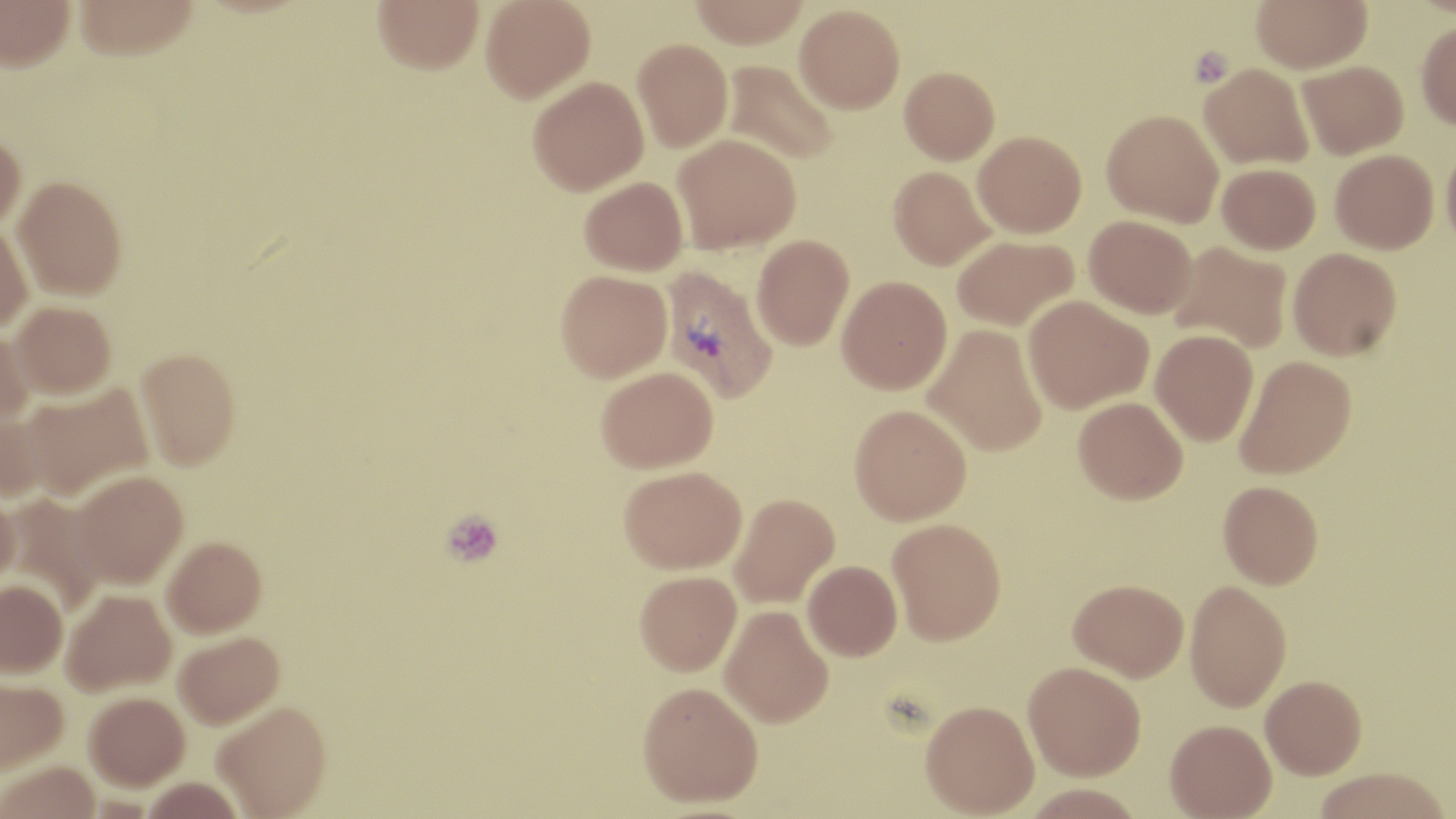
Approximate bounding boxes as (x1,y1)-(x2,y2) corner pairs in pixels. Uninfected red blood cell locations: (1,0)-(75,71), (72,0)-(199,61), (373,0)-(484,73), (481,0)-(595,102), (689,0)-(809,48), (1251,0)-(1372,73), (794,4)-(905,113), (1416,21)-(1456,130), (633,38)-(733,151), (722,60)-(839,165), (1298,60)-(1408,159), (1199,62)-(1314,169), (899,66)-(999,164), (527,75)-(648,195), (1102,108)-(1224,227), (973,130)-(1086,237), (0,131)-(26,234), (672,133)-(801,252), (1440,138)-(1456,254), (1330,149)-(1438,253), (1217,163)-(1321,254), (888,166)-(994,270), (13,175)-(127,298), (580,176)-(688,275), (1085,214)-(1197,318), (0,222)-(33,333), (752,234)-(854,350), (952,234)-(1078,331), (1169,241)-(1293,353), (1287,247)-(1402,360), (555,269)-(672,382), (837,275)-(952,394), (1023,295)-(1152,413), (11,301)-(116,399), (923,324)-(1047,455), (0,328)-(33,432), (1151,329)-(1259,446), (135,347)-(241,469), (1235,355)-(1356,479), (597,366)-(718,472), (23,384)-(153,502), (1074,397)-(1188,504), (849,404)-(972,525), (0,411)-(49,504), (619,465)-(747,574), (71,471)-(188,589), (1218,480)-(1323,589), (0,491)-(19,595), (729,492)-(840,608), (3,495)-(107,616), (887,518)-(1006,645), (162,537)-(267,638), (803,560)-(902,660), (635,570)-(742,675), (0,579)-(67,678), (1069,579)-(1188,681), (1185,580)-(1291,711), (61,589)-(176,697), (720,605)-(833,727), (173,632)-(285,730), (1023,661)-(1146,780), (1260,674)-(1366,778), (0,678)-(68,776), (638,681)-(763,807), (84,692)-(190,792), (920,700)-(1039,817), (212,703)-(333,819), (1165,719)-(1277,818), (1,762)-(101,819), (1313,767)-(1452,819). Plasmodium vivax-infected red blood cell locations: (660,265)-(778,403). Platelet locations: (1187,45)-(1235,88), (441,510)-(504,569). Slide-level diagnosis: Plasmodium vivax. Thin blood film. Captured at 1000x magnification. Light microscopy. Image is 1456×819 pixels. Single field of view. May-Grünwald-Giemsa-stained preparation.